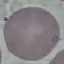 Malaria status: uninfected. Cell patch, automatically extracted from a larger field of view and resized to 64 × 64 pixels. Giemsa stain. Thin blood film. Photographed with a smartphone camera at the microscope eyepiece.